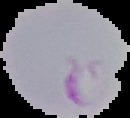

image_type: segmented cell region with the area outside set to black
image_size: 130×118 pixels
preparation: thin blood smear
malaria_status: parasitized